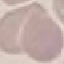
{
  "malaria_status": "uninfected",
  "stain": "Giemsa",
  "capture": "smartphone through the microscope eyepiece",
  "preparation": "thin blood smear",
  "image_type": "cell patch, automatically extracted from a larger field of view and resized to 64 × 64 pixels"
}